Describe the morphology of the red blood cells.
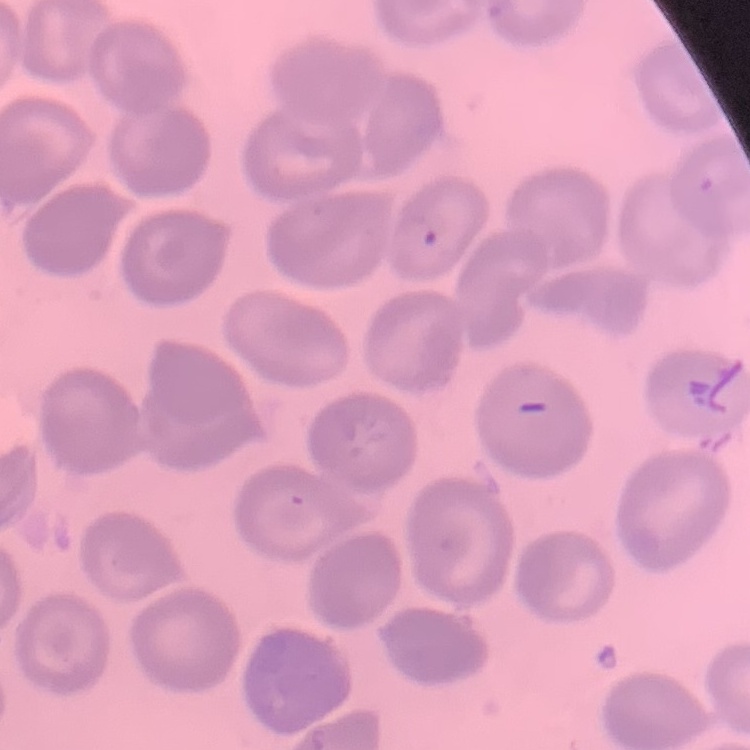
No rouleaux formation.

Summary:
  - Preparation: thin blood film
  - Image type: square crop of a larger photomicrograph
  - Stain: Field's or Giemsa